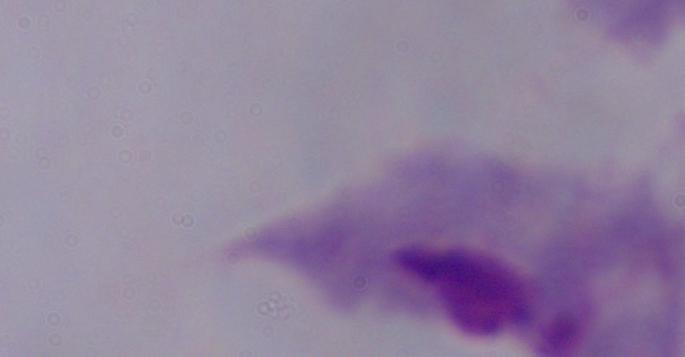
A trichomonad is seen. Micrograph. Captured at 1000x magnification.